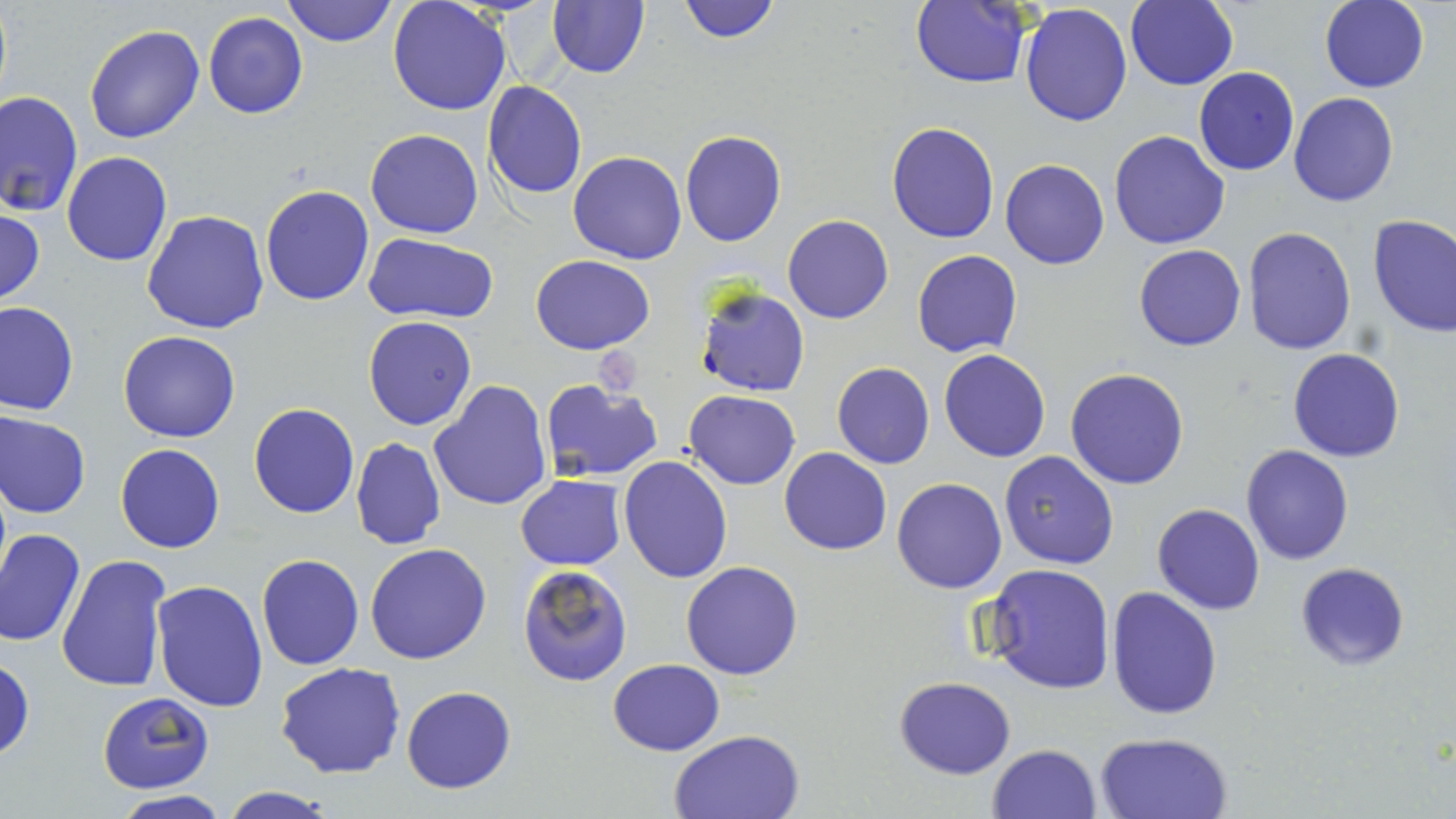
slide_level_diagnosis: Plasmodium falciparum
field_of_view: single
magnification: 1000x
plasmodium_falciparum_infected_red_blood_cell_locations: 'approximate bounding boxes as (x1, y1, x2, y2) in pixels: (695, 284, 810, 396)'
preparation: thin blood smear
stain: May-Grünwald-Giemsa
uninfected_red_blood_cell_locations: 'approximate bounding boxes as (x1, y1, x2, y2) in pixels: (280, 0, 398, 48), (388, 0, 510, 116), (678, 0, 781, 43), (1124, 0, 1239, 89), (545, 1, 651, 78), (912, 1, 1029, 87), (1319, 1, 1430, 94), (1019, 3, 1133, 127), (202, 11, 308, 119), (84, 25, 206, 144), (1194, 67, 1300, 176), (482, 81, 587, 200), (0, 89, 82, 217), (1288, 92, 1397, 208), (886, 121, 999, 244), (364, 128, 485, 238), (680, 130, 787, 247), (1108, 130, 1230, 250), (568, 151, 687, 264), (61, 152, 172, 267), (1001, 158, 1110, 269), (259, 184, 373, 306), (0, 207, 45, 308), (142, 208, 270, 334), (784, 214, 894, 323), (1367, 214, 1456, 339), (1242, 226, 1356, 356), (364, 233, 499, 323), (1134, 244, 1245, 350), (912, 249, 1022, 357), (532, 255, 655, 354), (0, 301, 79, 415), (363, 316, 476, 430), (117, 331, 242, 443), (938, 349, 1051, 462), (1287, 349, 1405, 462), (831, 362, 935, 470), (1064, 368, 1190, 490), (539, 378, 662, 484), (429, 380, 552, 511), (684, 391, 799, 490), (248, 403, 359, 519), (0, 411, 91, 519), (350, 437, 445, 550), (114, 444, 224, 554), (1240, 445, 1355, 565), (779, 446, 892, 556), (999, 451, 1119, 569), (618, 455, 732, 583), (516, 475, 626, 570), (891, 477, 1007, 594), (1152, 504, 1266, 616), (0, 529, 84, 646), (365, 543, 492, 665), (58, 553, 173, 695), (256, 553, 364, 671), (682, 561, 803, 680), (1295, 561, 1411, 671), (980, 563, 1116, 695), (517, 564, 633, 686), (153, 580, 269, 712), (1107, 586, 1222, 721), (0, 655, 34, 762), (606, 658, 725, 755), (275, 661, 405, 779), (895, 675, 1016, 778), (401, 685, 516, 793), (97, 691, 215, 794), (669, 729, 804, 818), (1093, 731, 1232, 819), (989, 742, 1102, 818), (218, 785, 337, 819), (110, 792, 233, 819)'
image_size: 1456×819 pixels
modality: light microscopy